Point out each malaria parasite.
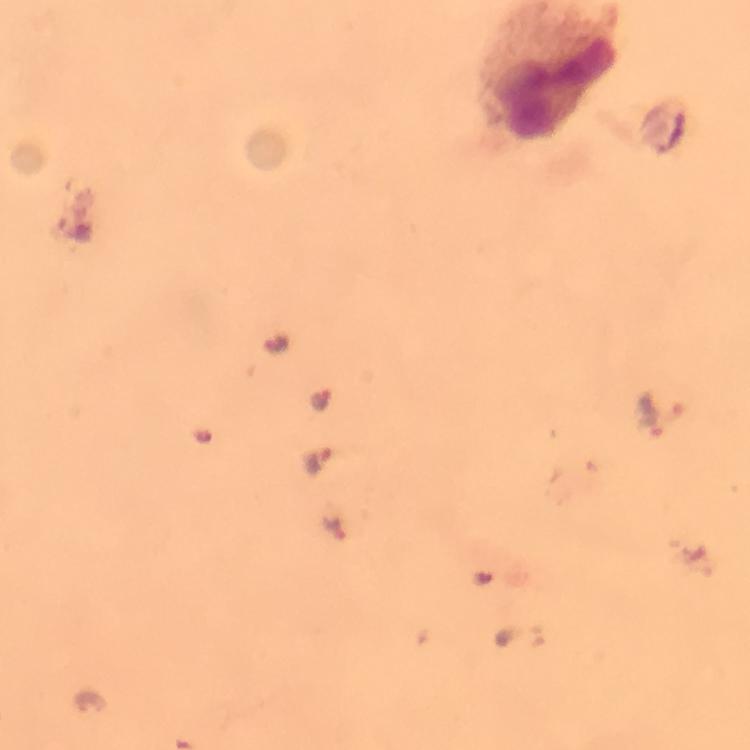
Approximate centers as (x, y) in pixels.
Malaria parasites: (75, 227), (321, 397), (319, 460), (333, 528).

cropped from = one field of view
magnification = 100x
preparation = thick blood film
immersion oil = applied
capture = smartphone camera through the microscope
image size = 750×750 pixels
stain = Giemsa
context = from a malaria diagnostic workup